State which parasite is depicted.
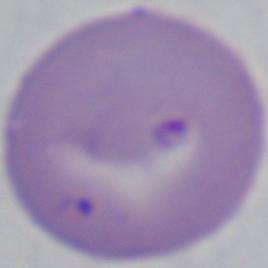

Babesia.

Summary:
  - Magnification: 1000x
  - Modality: photomicrograph